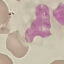

result: no malaria parasites seen
stain: Giemsa
image_type: cell patch, automatically extracted from a larger field of view and resized to 64 × 64 pixels
capture: smartphone through the microscope eyepiece
preparation: thin blood smear